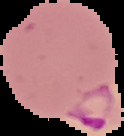

Image is 124×136 pixels. Cell region segmented out of the field of view; the surrounding area is masked to black. From a thin blood smear. Malaria status: parasitized.